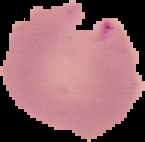 Result: malaria parasites identified. Cell region segmented out of the field of view; the surrounding area is masked to black. From a thin blood smear. Image is 145×142 pixels.